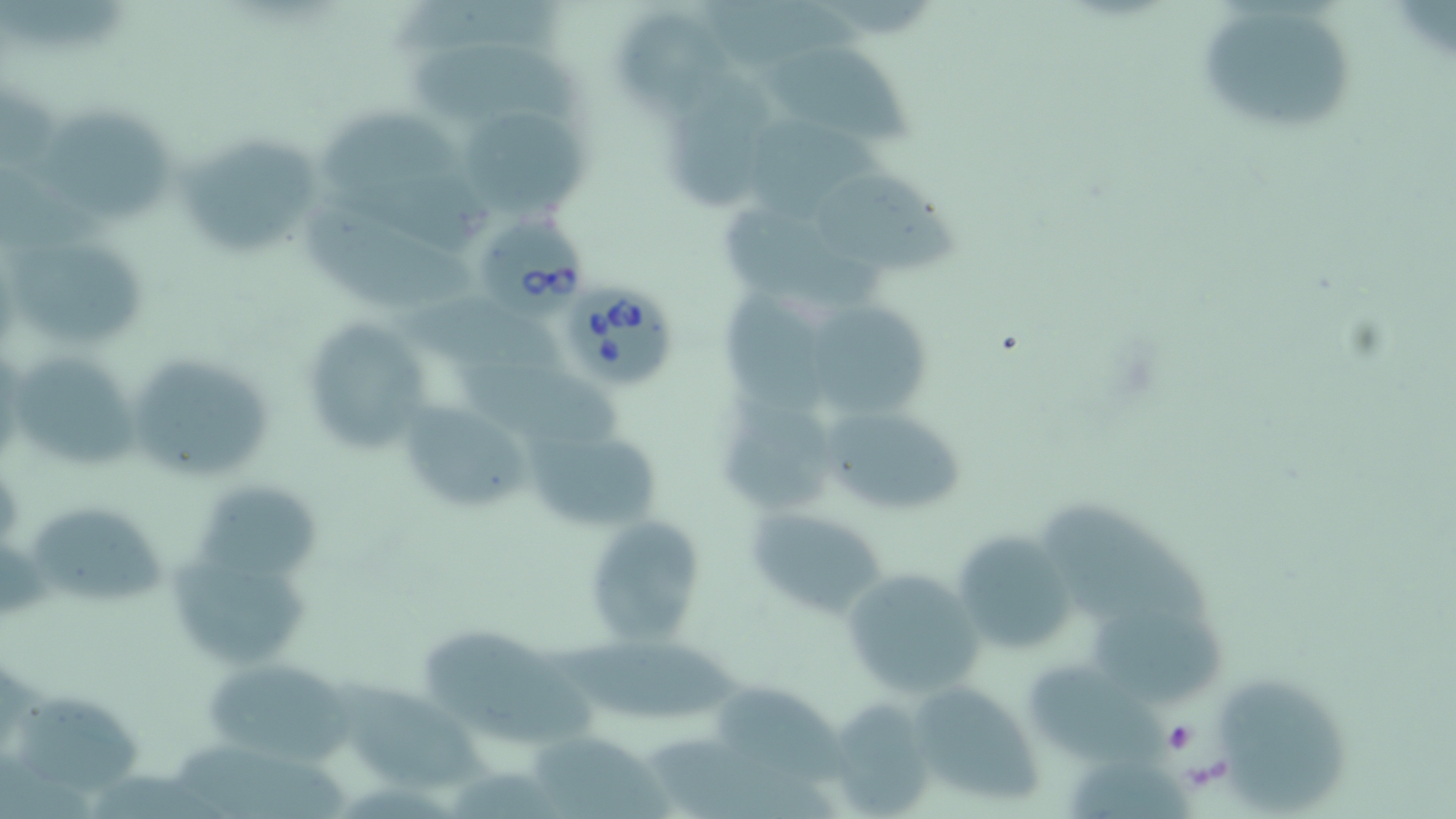
slide_level_diagnosis: Babesia divergens
image_size: 1456×819 pixels
field_of_view: one of a larger specimen
stain: May-Grünwald-Giemsa
babesia_divergens_infected_red_blood_cell_locations: 'approximate bounding boxes as (x1, y1, x2, y2) in pixels: (472, 207, 592, 321), (564, 283, 679, 389)'
uninfected_red_blood_cell_locations: 'approximate bounding boxes as (x1, y1, x2, y2) in pixels: (702, 0, 870, 73), (1194, 2, 1362, 137), (613, 11, 747, 117), (754, 34, 920, 140), (405, 44, 591, 129), (664, 76, 771, 215), (33, 101, 172, 221), (318, 106, 459, 190), (466, 111, 587, 215), (744, 121, 901, 218), (175, 132, 316, 254), (808, 163, 966, 273), (296, 198, 483, 313), (720, 201, 882, 312), (8, 236, 150, 343), (719, 284, 839, 413), (410, 293, 562, 370), (816, 306, 932, 417), (295, 315, 433, 455), (126, 351, 276, 486), (13, 355, 137, 467), (451, 359, 624, 449), (397, 400, 528, 516), (719, 400, 850, 514), (826, 412, 962, 518), (522, 430, 661, 525), (190, 484, 319, 581), (26, 498, 169, 603), (1040, 498, 1221, 642), (746, 502, 896, 624), (583, 515, 705, 647), (951, 529, 1077, 659), (179, 559, 311, 669), (840, 566, 985, 697), (1094, 604, 1229, 707), (420, 633, 604, 746), (542, 635, 748, 720), (204, 659, 352, 765), (1028, 662, 1176, 771), (1214, 673, 1352, 815), (327, 675, 491, 791), (721, 681, 853, 783), (907, 682, 1040, 806), (12, 688, 149, 794), (832, 701, 935, 815), (529, 731, 671, 819), (649, 732, 836, 819), (179, 735, 350, 819)'
magnification: 1000x
modality: light microscopy
preparation: thin blood film